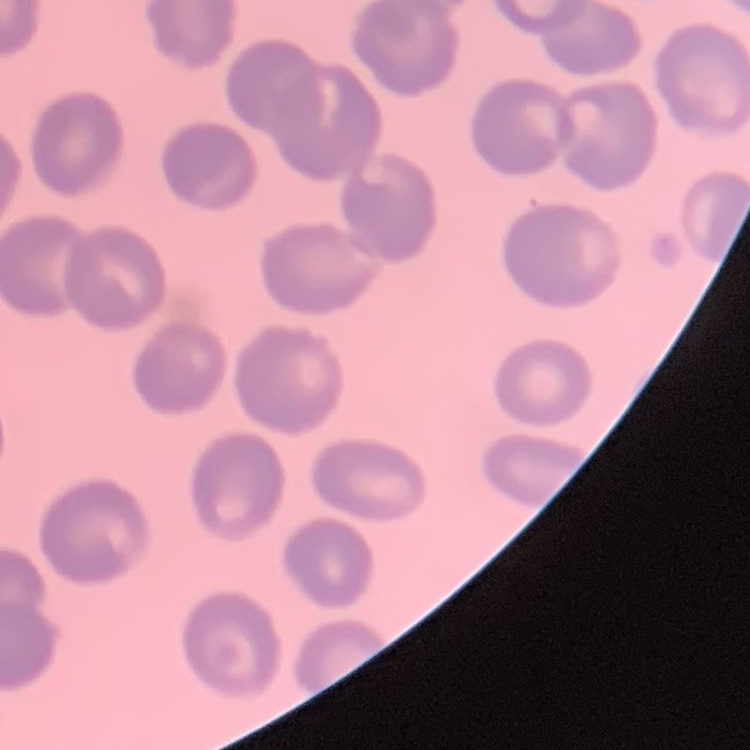

The red blood cells show no rouleaux formation. Square crop of a larger photomicrograph. Stained with either Field's or Giemsa. Thin peripheral smear.